Classify this cell by malaria status.
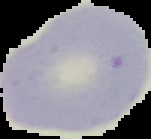
Uninfected.

Summary:
  - Preparation: thin blood film
  - Image type: segmented cell region with the area outside set to black
  - Image size: 151×139 pixels